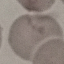

result = no malaria parasites detected
stain = Giemsa
capture = smartphone through the microscope eyepiece
image type = cell patch, automatically extracted from a larger field of view and resized to 64 × 64 pixels
preparation = thin blood film